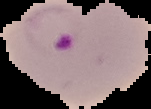
Summary:
  - Result: malaria parasites detected
  - Image size: 151×109 pixels
  - Image type: cell region segmented out of the field of view; surrounding area masked to black
  - Preparation: thin blood film